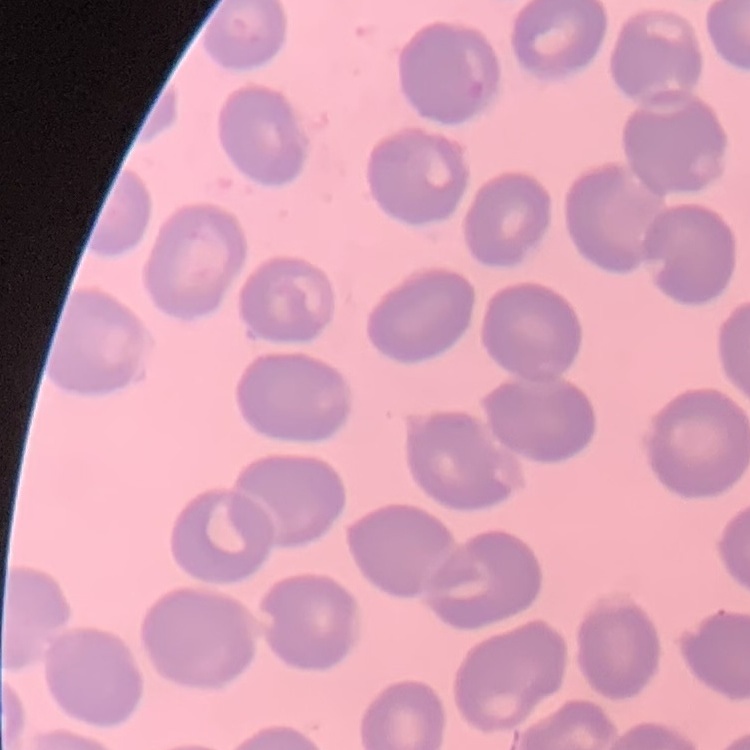
The red blood cells show no rouleaux formation. Thin peripheral smear. Field's or Giemsa stain. Square crop of a larger photomicrograph.